Assess this cell for malaria.
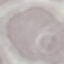
Uninfected.

Acquired by smartphone through the microscope eyepiece. Thin blood smear. Automatically extracted cell patch, resized to 64 × 64 pixels. Giemsa-stained preparation.